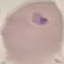

Malaria status: uninfected. Automatically extracted cell patch, resized to 64 × 64 pixels. Thin blood smear. Giemsa stain. Photographed with a smartphone camera at the microscope eyepiece.